Outline each blood parasite and name the species.
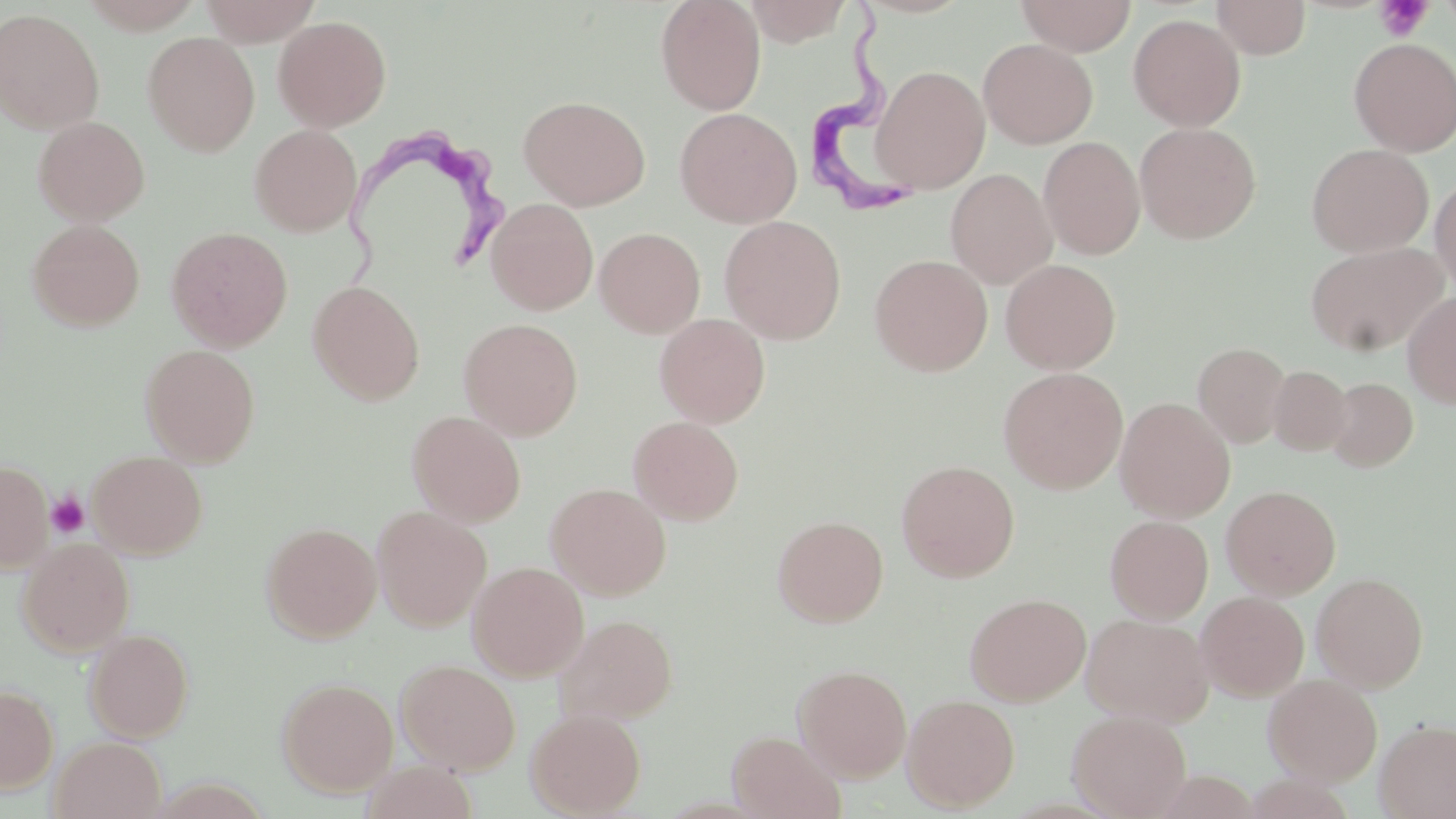

Approximate bounding boxes as [x1, y1, x2, y2] in pixels.
Trypanosoma brucei: [806, 0, 918, 220], [340, 125, 511, 290].
No Plasmodium falciparum, Plasmodium ovale, Plasmodium malariae, Plasmodium vivax, or Babesia divergens observed.

Platelet locations: [1375, 0, 1432, 42], [47, 491, 89, 538]. Uninfected red blood cell locations: [656, 0, 766, 114], [1015, 0, 1137, 56], [198, 1, 321, 45], [745, 1, 855, 46], [1212, 1, 1311, 59], [1, 8, 105, 134], [1129, 13, 1246, 131], [273, 15, 392, 132], [143, 32, 260, 156], [1349, 37, 1456, 156], [978, 38, 1098, 149], [871, 65, 990, 194], [519, 95, 650, 211], [675, 107, 802, 228], [33, 115, 150, 226], [1134, 122, 1261, 244], [249, 125, 362, 236], [1039, 136, 1145, 260], [1306, 143, 1433, 258], [946, 168, 1058, 289], [1430, 171, 1456, 295], [486, 198, 598, 315], [719, 215, 847, 344], [27, 219, 145, 331], [166, 226, 293, 351], [594, 227, 705, 338], [1306, 241, 1448, 356], [869, 254, 993, 376], [1000, 259, 1120, 374], [308, 281, 425, 406], [1402, 291, 1456, 410], [655, 313, 770, 427], [459, 318, 583, 440], [1193, 342, 1291, 448], [139, 343, 261, 466], [1268, 364, 1353, 455], [998, 367, 1128, 494], [1323, 377, 1418, 471], [1115, 397, 1235, 522], [407, 410, 526, 526], [628, 416, 744, 525], [87, 450, 207, 559], [0, 460, 53, 572], [896, 460, 1020, 582], [546, 483, 671, 599], [1221, 485, 1341, 599], [372, 506, 491, 631], [772, 515, 889, 627], [1105, 515, 1213, 623], [261, 521, 382, 643], [17, 537, 135, 657], [467, 561, 589, 681], [1312, 572, 1429, 692], [1195, 591, 1310, 701], [964, 592, 1091, 705], [1081, 613, 1214, 727], [555, 614, 678, 725], [84, 628, 194, 742], [396, 659, 521, 774], [792, 663, 912, 781], [1263, 674, 1382, 786], [277, 677, 399, 797], [0, 684, 58, 793], [902, 693, 1020, 812], [525, 708, 647, 817], [1067, 709, 1192, 819], [1374, 718, 1456, 819], [727, 730, 847, 819], [50, 736, 166, 819], [360, 760, 479, 819]. Slide-level diagnosis: Trypanosoma brucei. Thin blood smear. Optical microscopy. Image is 1456×819 pixels. May-Grünwald-Giemsa-stained preparation. Captured at 1000x magnification. One field of a larger specimen.